Comment on the morphology of the erythrocytes.
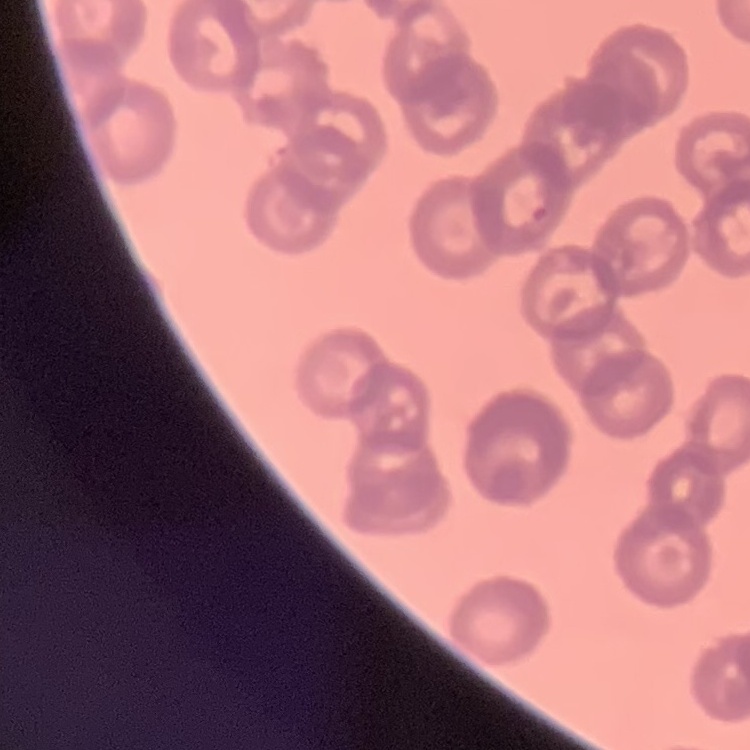

They show rouleaux formation.

Stained with either Field's or Giemsa. Thin blood smear. Square crop of a larger photomicrograph.